Give the position of every leukocyte visible.
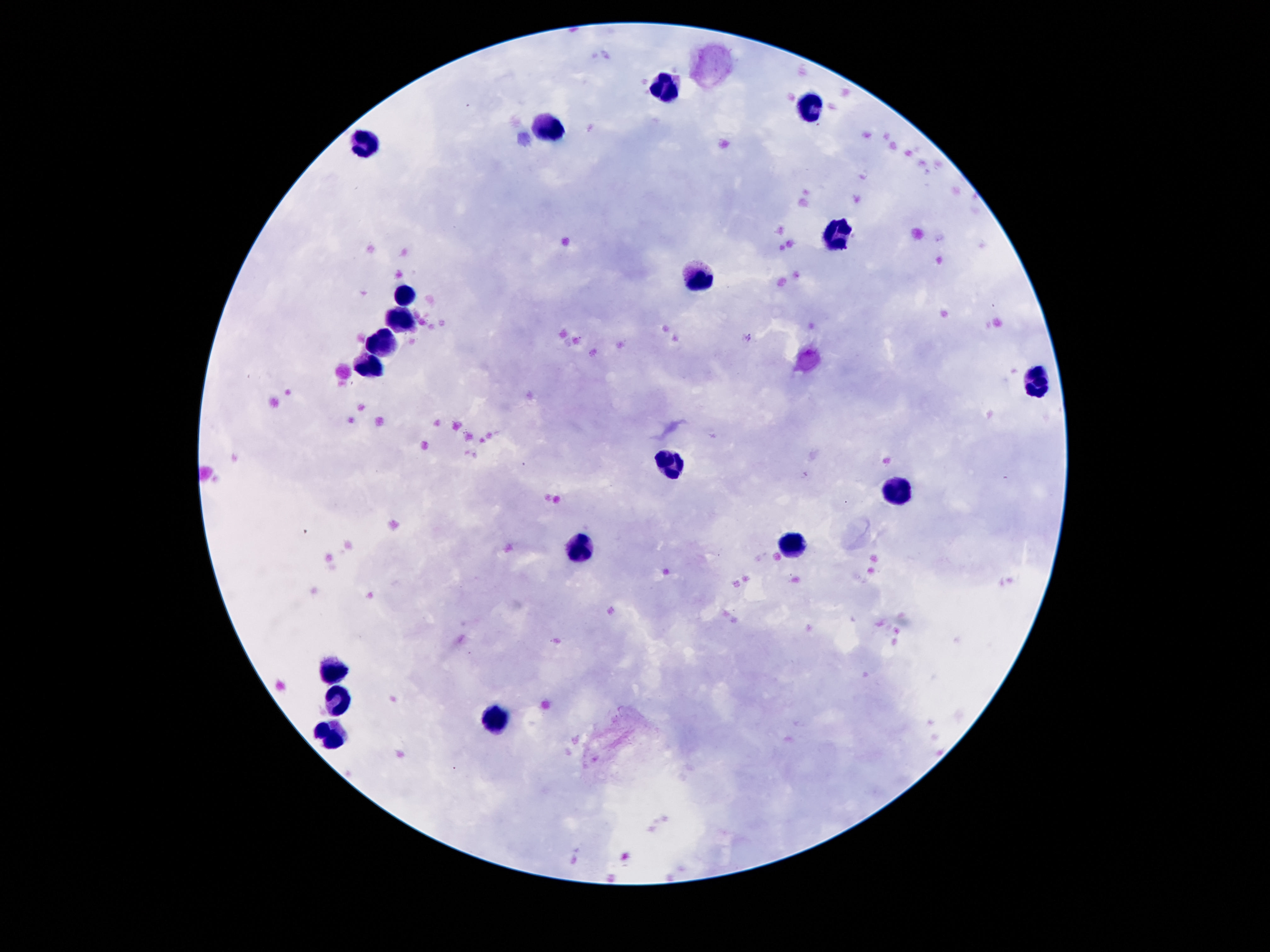
Approximate centers as (x, y) in pixels.
Leukocytes: (668, 93), (813, 106), (548, 135), (365, 145), (836, 236), (701, 278), (403, 292), (401, 318), (384, 341), (372, 366), (1035, 380), (670, 460), (897, 494), (794, 546), (582, 551), (332, 673), (336, 697), (494, 722), (328, 738).

100x magnification. Thick blood film. Image is 1270×952 pixels. Patient malaria status: not infected. Giemsa-stained preparation. Single field of view. Smartphone photograph taken through the microscope eyepiece.